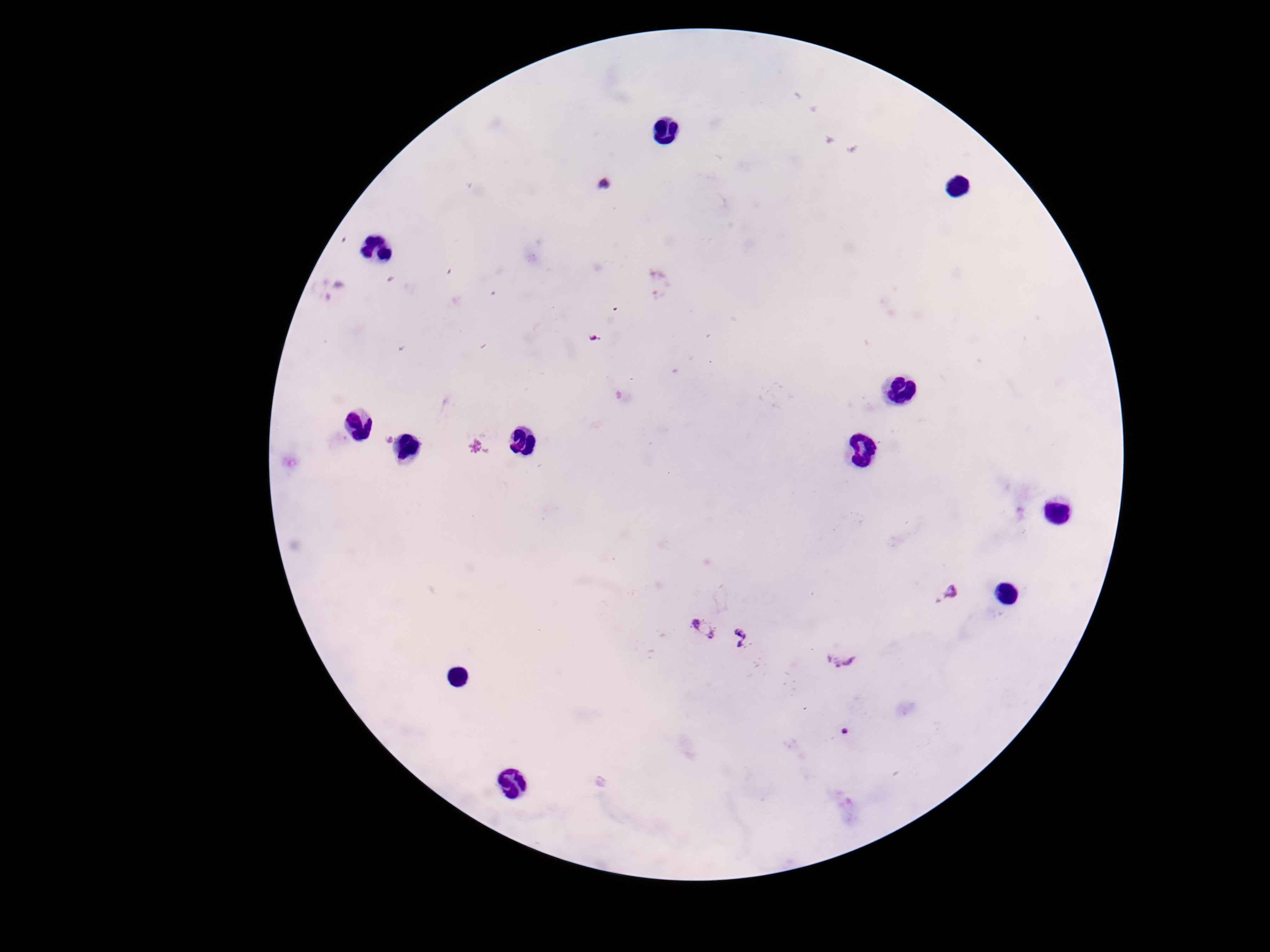

Approximate centers as [x, y] in pixels. Plasmodium parasite locations: [603, 184], [596, 338], [385, 438], [476, 445], [951, 592], [701, 624], [746, 641], [843, 658], [845, 730]. 100x magnification. Photographed through the microscope eyepiece with a smartphone camera. Thick blood film. Patient malaria status: infected. Image is 1270×952 pixels. Single field of view. Giemsa-stained preparation.